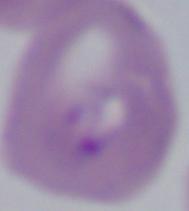 Captured at 1000x magnification. Photomicrograph. A Babesia parasite is shown.